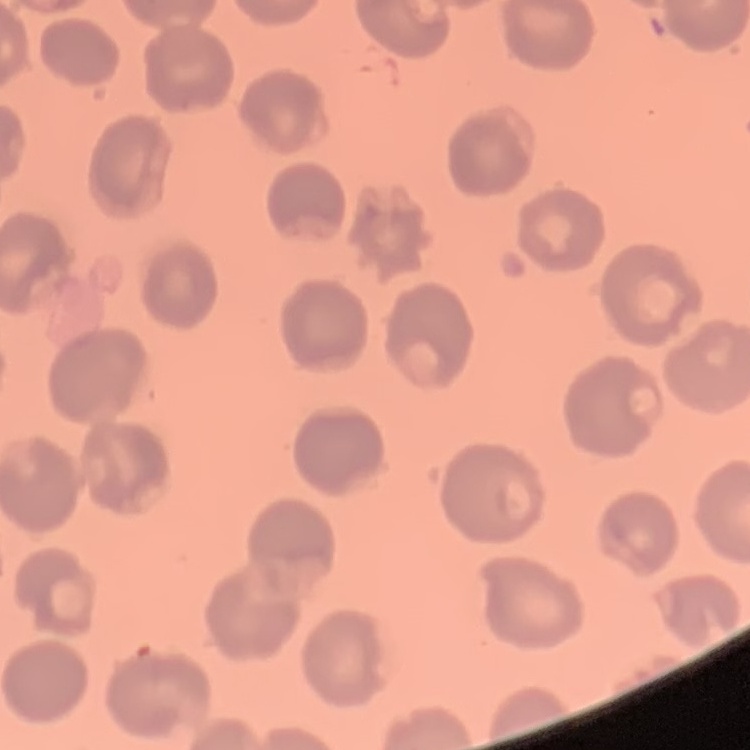

red blood cell morphology = no rouleaux formation
preparation = thin blood film
stain = Field's or Giemsa
image type = square crop of a larger photomicrograph